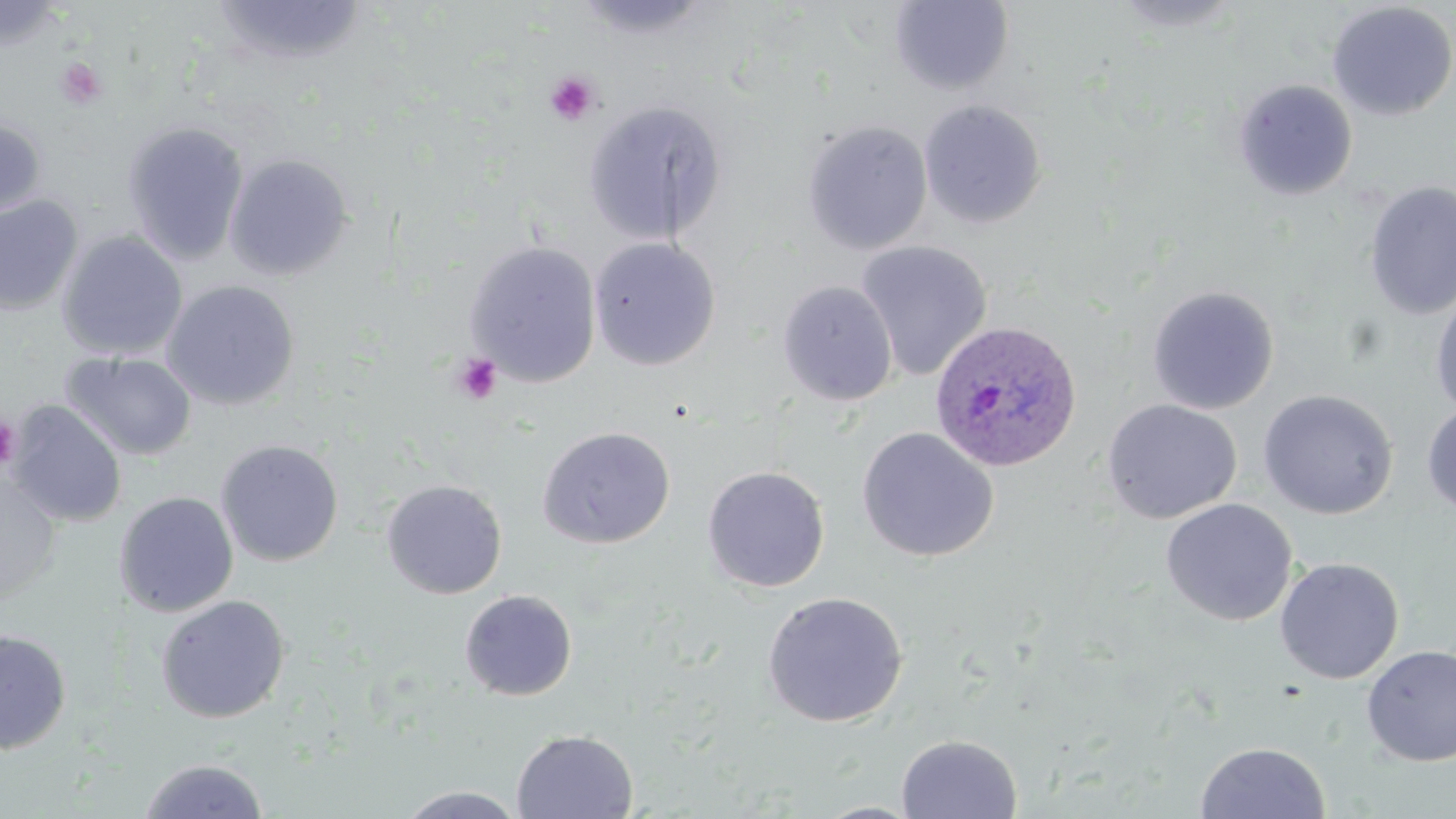

Summary:
  - Coordinate format: approximate bounding boxes as named x1/y1/x2/y2 corners in pixels
  - Uninfected red blood cell locations: (x1=211, y1=0, x2=367, y2=67), (x1=571, y1=0, x2=714, y2=40), (x1=1108, y1=0, x2=1248, y2=34), (x1=889, y1=1, x2=1014, y2=95), (x1=0, y1=2, x2=69, y2=51), (x1=1326, y1=2, x2=1456, y2=121), (x1=1232, y1=79, x2=1358, y2=201), (x1=583, y1=99, x2=728, y2=245), (x1=918, y1=100, x2=1047, y2=229), (x1=0, y1=118, x2=47, y2=219), (x1=802, y1=120, x2=933, y2=255), (x1=123, y1=122, x2=249, y2=265), (x1=224, y1=153, x2=354, y2=281), (x1=1363, y1=180, x2=1456, y2=321), (x1=0, y1=195, x2=83, y2=315), (x1=57, y1=231, x2=188, y2=360), (x1=589, y1=237, x2=721, y2=370), (x1=855, y1=240, x2=993, y2=381), (x1=464, y1=241, x2=602, y2=386), (x1=161, y1=280, x2=300, y2=411), (x1=777, y1=281, x2=898, y2=406), (x1=1146, y1=285, x2=1279, y2=415), (x1=1430, y1=287, x2=1456, y2=420), (x1=62, y1=351, x2=197, y2=461), (x1=1258, y1=389, x2=1398, y2=519), (x1=1102, y1=399, x2=1242, y2=524), (x1=7, y1=401, x2=127, y2=527), (x1=1421, y1=401, x2=1456, y2=518), (x1=536, y1=426, x2=676, y2=549), (x1=856, y1=427, x2=999, y2=563), (x1=215, y1=439, x2=344, y2=567), (x1=702, y1=465, x2=830, y2=593), (x1=0, y1=475, x2=63, y2=603), (x1=381, y1=479, x2=507, y2=599), (x1=114, y1=491, x2=239, y2=617), (x1=1160, y1=498, x2=1298, y2=627), (x1=1274, y1=557, x2=1404, y2=684), (x1=459, y1=589, x2=578, y2=701), (x1=762, y1=591, x2=908, y2=728), (x1=155, y1=594, x2=290, y2=724), (x1=0, y1=628, x2=72, y2=754), (x1=1361, y1=645, x2=1456, y2=766), (x1=511, y1=729, x2=638, y2=818), (x1=895, y1=734, x2=1023, y2=818), (x1=1195, y1=742, x2=1330, y2=819), (x1=138, y1=757, x2=270, y2=818), (x1=395, y1=786, x2=527, y2=819), (x1=810, y1=801, x2=926, y2=818)
  - Plasmodium ovale-infected red blood cell locations: (x1=928, y1=319, x2=1083, y2=473)
  - Platelet locations: (x1=55, y1=56, x2=109, y2=110), (x1=545, y1=71, x2=601, y2=126), (x1=450, y1=352, x2=504, y2=405), (x1=0, y1=417, x2=20, y2=470)
  - Slide-level diagnosis: Plasmodium ovale
  - Preparation: thin blood film
  - Stain: May-Grünwald-Giemsa
  - Modality: optical microscopy
  - Image size: 1456×819 pixels
  - Magnification: 1000x
  - Field of view: single